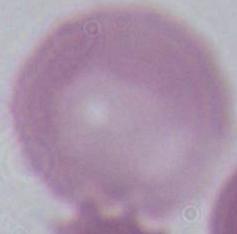
Summary:
  - Magnification: 1000x
  - Modality: micrograph
  - Identification: red blood cell